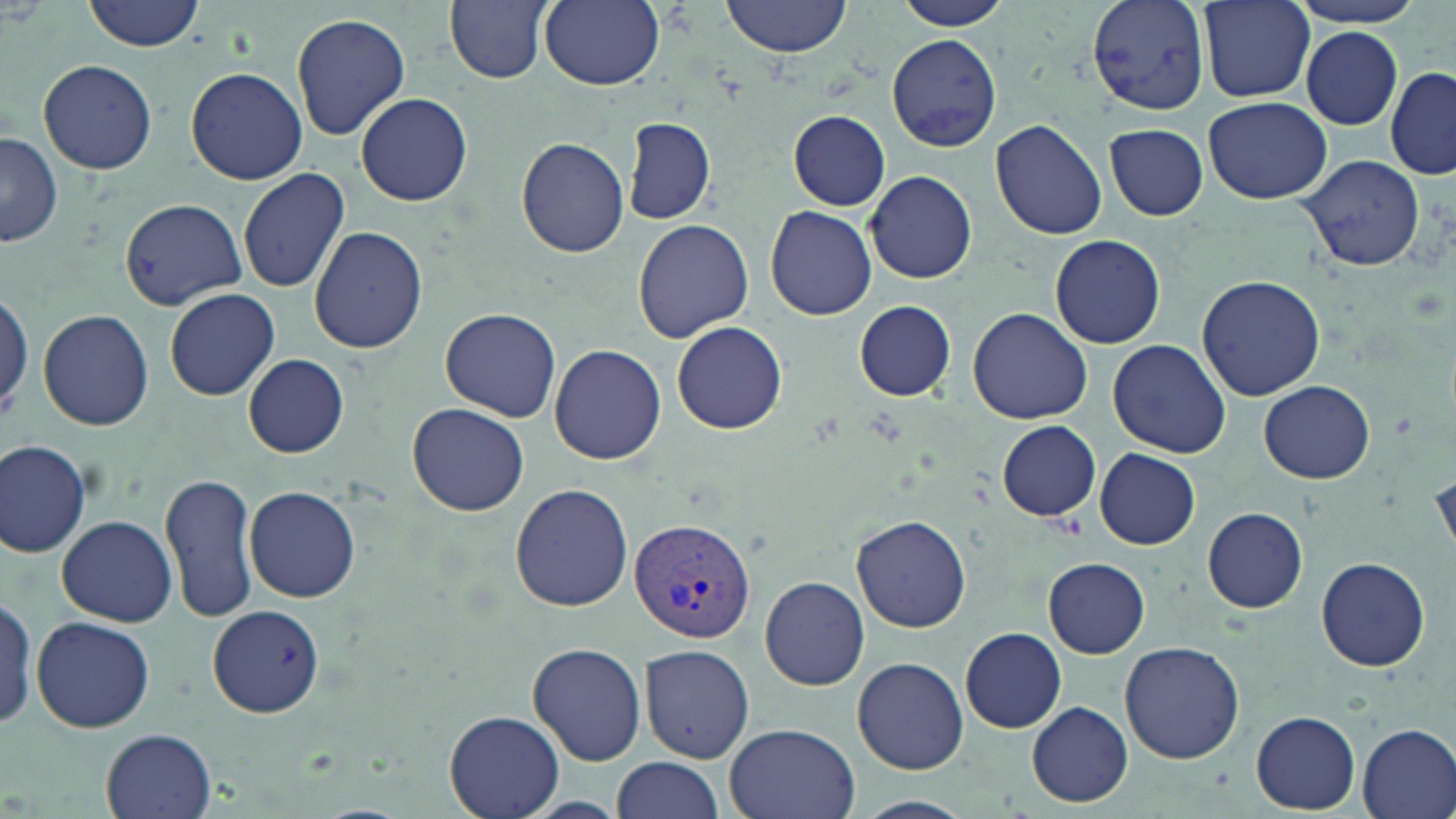

Summary:
  - Coordinate format: approximate bounding boxes as [x1, y1, x2, y2] in pixels
  - Plasmodium vivax-infected red blood cell locations: [629, 516, 755, 647]
  - Uninfected red blood cell locations: [84, 0, 207, 53], [445, 0, 552, 84], [539, 0, 664, 89], [722, 0, 850, 57], [897, 0, 1013, 30], [1088, 0, 1211, 115], [1197, 0, 1317, 102], [1289, 0, 1429, 29], [291, 12, 411, 140], [1300, 28, 1404, 130], [885, 33, 1001, 152], [38, 60, 158, 174], [1384, 64, 1456, 181], [185, 68, 308, 183], [356, 92, 473, 206], [1203, 96, 1331, 204], [788, 111, 891, 209], [623, 115, 715, 225], [991, 118, 1107, 240], [1105, 124, 1208, 220], [0, 132, 61, 248], [516, 136, 629, 258], [1298, 153, 1427, 273], [238, 167, 350, 292], [865, 171, 977, 283], [120, 198, 249, 312], [765, 206, 878, 320], [633, 216, 755, 342], [310, 227, 429, 355], [1050, 233, 1167, 349], [1197, 275, 1324, 400], [0, 283, 33, 421], [164, 287, 281, 400], [855, 300, 956, 400], [969, 306, 1092, 423], [441, 307, 561, 422], [37, 309, 154, 430], [672, 321, 787, 434], [1108, 340, 1232, 460], [550, 343, 667, 464], [243, 353, 349, 457], [1259, 380, 1375, 484], [407, 401, 530, 516], [997, 421, 1099, 521], [0, 437, 93, 559], [1095, 448, 1200, 549], [1430, 460, 1455, 564], [160, 470, 260, 622], [244, 483, 362, 603], [510, 483, 633, 612], [1202, 506, 1308, 613], [57, 514, 177, 626], [853, 515, 971, 633], [1317, 556, 1431, 671], [1044, 557, 1151, 657], [760, 575, 870, 690], [0, 596, 41, 731], [204, 605, 325, 716], [31, 615, 155, 733], [961, 627, 1065, 732], [1120, 640, 1244, 763], [527, 641, 647, 765], [640, 645, 757, 762], [853, 656, 968, 774], [470, 666, 628, 795], [1027, 702, 1132, 806], [445, 710, 562, 819], [1251, 711, 1360, 813], [721, 723, 861, 819], [1355, 723, 1456, 819], [100, 729, 216, 819], [613, 756, 723, 818], [855, 796, 974, 819]
  - Slide-level diagnosis: Plasmodium vivax
  - Field of view: one of a larger specimen
  - Stain: May-Grünwald-Giemsa
  - Magnification: 1000x
  - Modality: light microscopy
  - Preparation: thin blood smear
  - Image size: 1456×819 pixels